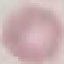
malaria_status: uninfected
capture: smartphone camera at the microscope eyepiece
stain: Giemsa
image_type: automatically extracted cell patch, resized to 64 × 64 pixels
preparation: thin blood film